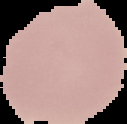

{
  "image_size": "127×124 pixels",
  "malaria_status": "uninfected",
  "image_type": "cell region segmented out of the field of view; surrounding area masked to black",
  "preparation": "thin blood smear"
}